Give the position of every malaria parasite.
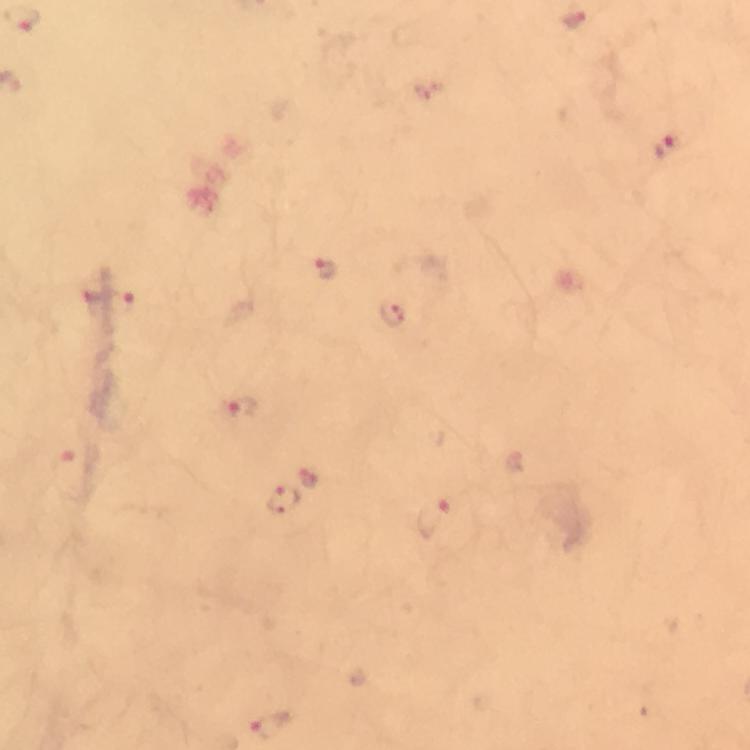
Approximate centers as (x, y) in pixels.
Malaria parasites: (666, 147), (325, 269), (120, 303), (393, 314), (242, 409), (63, 460), (308, 479), (282, 501), (433, 518), (272, 726).

preparation = thick blood film
stain = Giemsa
immersion oil = used
image size = 750×750 pixels
cropped from = a single field of view
magnification = 100x
context = from a malaria diagnostic workup
capture = smartphone mounted on the microscope